Locate and identify every blood parasite.
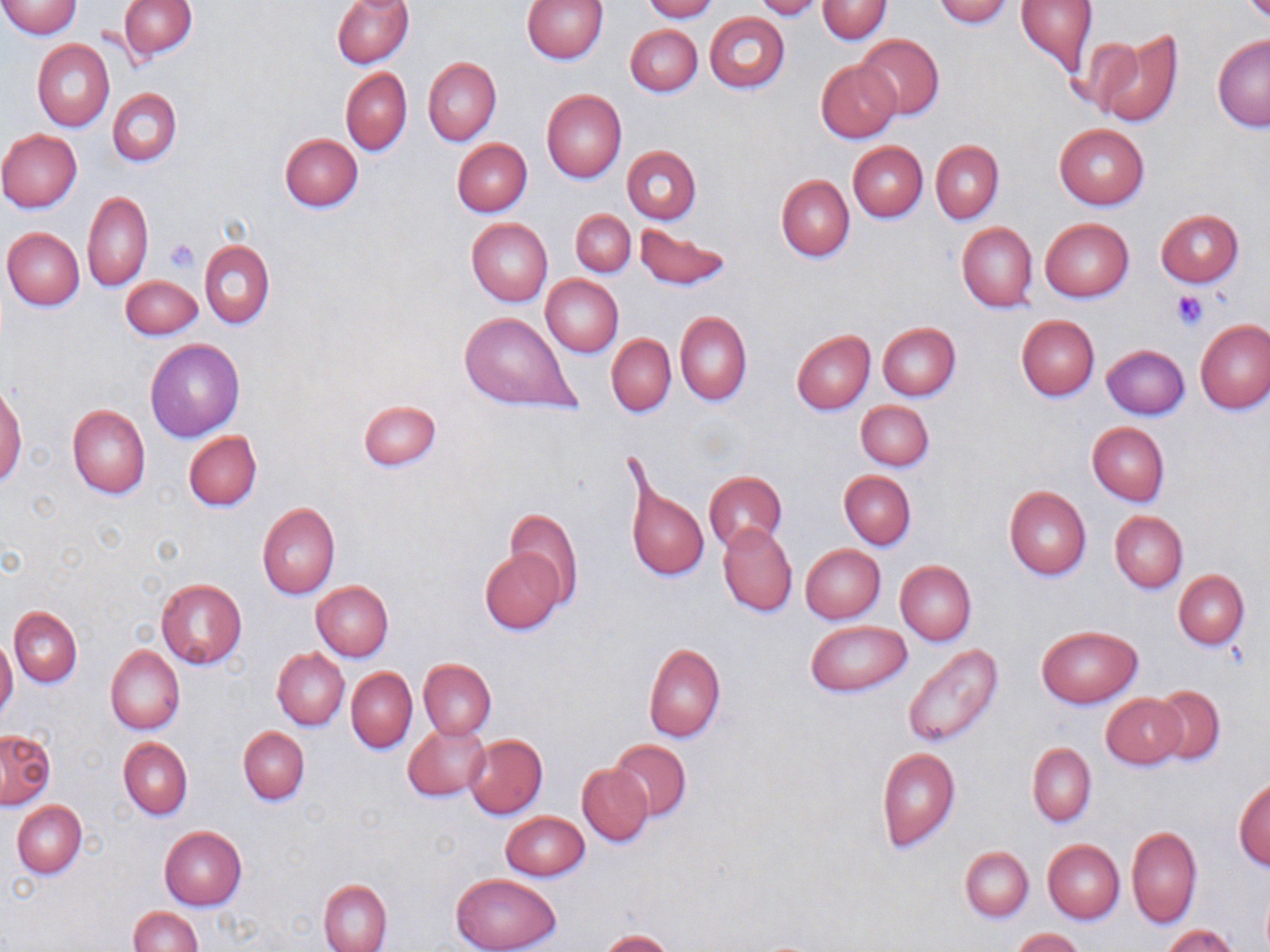

No blood parasites observed.

Summary:
  - Coordinate format: approximate bounding boxes as named x1/y1/x2/y2 corners in pixels
  - Uninfected red blood cell locations: (x1=0, y1=0, x2=82, y2=38), (x1=332, y1=0, x2=414, y2=68), (x1=522, y1=0, x2=608, y2=65), (x1=643, y1=0, x2=718, y2=22), (x1=753, y1=0, x2=827, y2=20), (x1=933, y1=0, x2=1014, y2=27), (x1=1015, y1=0, x2=1098, y2=74), (x1=119, y1=1, x2=195, y2=58), (x1=817, y1=1, x2=891, y2=43), (x1=704, y1=12, x2=790, y2=93), (x1=625, y1=25, x2=701, y2=96), (x1=1093, y1=29, x2=1186, y2=129), (x1=856, y1=34, x2=944, y2=121), (x1=1212, y1=35, x2=1270, y2=132), (x1=33, y1=39, x2=115, y2=131), (x1=424, y1=56, x2=501, y2=145), (x1=816, y1=59, x2=900, y2=142), (x1=341, y1=67, x2=413, y2=155), (x1=108, y1=88, x2=182, y2=166), (x1=541, y1=89, x2=626, y2=183), (x1=1053, y1=124, x2=1150, y2=209), (x1=0, y1=129, x2=83, y2=212), (x1=280, y1=132, x2=363, y2=212), (x1=452, y1=138, x2=532, y2=216), (x1=932, y1=141, x2=1004, y2=222), (x1=847, y1=142, x2=927, y2=221), (x1=623, y1=146, x2=702, y2=223), (x1=776, y1=175, x2=855, y2=262), (x1=83, y1=192, x2=153, y2=291), (x1=571, y1=209, x2=635, y2=276), (x1=1155, y1=209, x2=1245, y2=287), (x1=466, y1=218, x2=553, y2=306), (x1=1040, y1=218, x2=1134, y2=301), (x1=634, y1=223, x2=729, y2=289), (x1=956, y1=223, x2=1038, y2=312), (x1=2, y1=227, x2=85, y2=311), (x1=199, y1=240, x2=275, y2=329), (x1=120, y1=275, x2=203, y2=339), (x1=541, y1=275, x2=624, y2=357), (x1=675, y1=311, x2=751, y2=405), (x1=459, y1=312, x2=580, y2=413), (x1=1016, y1=314, x2=1100, y2=401), (x1=1196, y1=319, x2=1270, y2=414), (x1=877, y1=322, x2=960, y2=401), (x1=792, y1=329, x2=875, y2=414), (x1=607, y1=334, x2=675, y2=417), (x1=146, y1=339, x2=244, y2=442), (x1=1102, y1=345, x2=1189, y2=420), (x1=0, y1=381, x2=27, y2=487), (x1=357, y1=399, x2=443, y2=470), (x1=856, y1=400, x2=933, y2=471), (x1=67, y1=403, x2=150, y2=499), (x1=1087, y1=421, x2=1169, y2=505), (x1=184, y1=430, x2=262, y2=511), (x1=623, y1=467, x2=710, y2=586), (x1=839, y1=470, x2=916, y2=550), (x1=704, y1=471, x2=787, y2=552), (x1=1004, y1=486, x2=1091, y2=580), (x1=257, y1=503, x2=339, y2=599), (x1=504, y1=507, x2=582, y2=606), (x1=1110, y1=511, x2=1188, y2=593), (x1=719, y1=524, x2=797, y2=616), (x1=801, y1=544, x2=886, y2=623), (x1=480, y1=549, x2=566, y2=633), (x1=896, y1=561, x2=976, y2=644), (x1=1172, y1=570, x2=1249, y2=649), (x1=156, y1=578, x2=247, y2=668), (x1=312, y1=580, x2=393, y2=661), (x1=9, y1=607, x2=83, y2=687), (x1=806, y1=620, x2=911, y2=697), (x1=1036, y1=625, x2=1142, y2=707), (x1=0, y1=638, x2=18, y2=721), (x1=902, y1=643, x2=1004, y2=748), (x1=644, y1=644, x2=726, y2=742), (x1=106, y1=645, x2=185, y2=734), (x1=273, y1=648, x2=349, y2=729), (x1=419, y1=658, x2=496, y2=740), (x1=347, y1=668, x2=417, y2=752), (x1=1151, y1=685, x2=1226, y2=764), (x1=1102, y1=693, x2=1185, y2=767), (x1=403, y1=725, x2=488, y2=799), (x1=238, y1=727, x2=310, y2=804), (x1=1, y1=729, x2=55, y2=808), (x1=464, y1=733, x2=548, y2=819), (x1=119, y1=738, x2=192, y2=819), (x1=608, y1=738, x2=691, y2=822), (x1=1028, y1=743, x2=1096, y2=825), (x1=875, y1=746, x2=961, y2=852), (x1=577, y1=763, x2=653, y2=845), (x1=1233, y1=777, x2=1270, y2=870), (x1=12, y1=800, x2=87, y2=878), (x1=501, y1=810, x2=589, y2=881), (x1=159, y1=827, x2=246, y2=910), (x1=1127, y1=827, x2=1202, y2=928), (x1=1049, y1=833, x2=1198, y2=926), (x1=1043, y1=840, x2=1125, y2=923), (x1=960, y1=846, x2=1032, y2=921), (x1=452, y1=873, x2=561, y2=952), (x1=319, y1=879, x2=391, y2=952), (x1=1260, y1=886, x2=1270, y2=952), (x1=128, y1=906, x2=201, y2=952), (x1=1161, y1=925, x2=1241, y2=952), (x1=1012, y1=928, x2=1086, y2=952), (x1=600, y1=930, x2=676, y2=952)
  - Platelet locations: (x1=166, y1=239, x2=198, y2=273), (x1=1171, y1=289, x2=1209, y2=330)
  - Slide-level diagnosis: no evidence of blood parasites
  - Preparation: thin blood film
  - Modality: light microscopy
  - Image size: 1270×952 pixels
  - Stain: May-Grünwald-Giemsa
  - Field of view: one of a larger specimen
  - Magnification: 1000x